Outline each blood parasite and name the species.
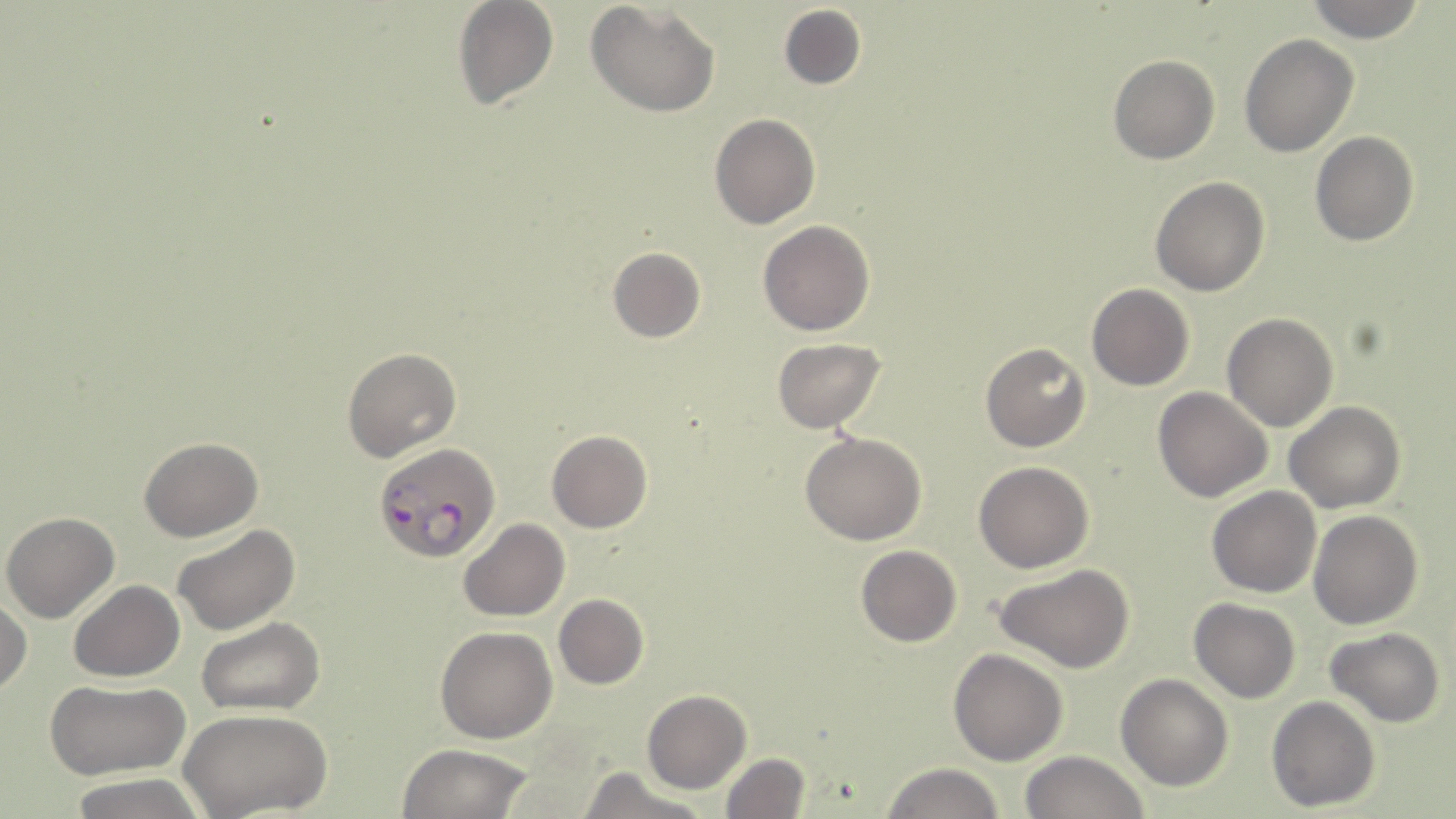
Approximate bounding boxes as [x1, y1, x2, y2] in pixels.
Plasmodium falciparum-infected red blood cells: [371, 442, 501, 562].
No Plasmodium ovale, Plasmodium malariae, Plasmodium vivax, Babesia divergens, or Trypanosoma brucei observed.

Uninfected red blood cell locations: [450, 0, 560, 110], [586, 0, 722, 117], [1307, 0, 1428, 43], [777, 3, 866, 90], [1239, 33, 1358, 157], [1108, 55, 1219, 165], [708, 113, 821, 229], [1310, 132, 1418, 246], [1149, 176, 1271, 297], [757, 220, 875, 336], [609, 247, 707, 343], [1086, 283, 1195, 391], [1223, 312, 1338, 431], [772, 337, 888, 434], [979, 342, 1092, 452], [341, 348, 462, 463], [1152, 386, 1272, 502], [1285, 400, 1404, 513], [547, 430, 652, 532], [800, 430, 927, 546], [140, 436, 264, 541], [973, 461, 1094, 572], [1207, 486, 1322, 598], [1308, 510, 1423, 629], [1, 511, 120, 623], [460, 518, 569, 621], [173, 523, 301, 636], [855, 545, 962, 648], [995, 565, 1134, 673], [69, 580, 184, 682], [553, 594, 650, 690], [0, 595, 30, 699], [1189, 600, 1300, 703], [197, 617, 326, 716], [435, 626, 557, 743], [1324, 628, 1447, 727], [949, 648, 1069, 766], [1116, 673, 1232, 790], [44, 678, 191, 781], [642, 690, 751, 794], [1267, 695, 1380, 811], [180, 708, 332, 817], [395, 742, 536, 819], [1018, 751, 1148, 819], [718, 752, 813, 819], [883, 763, 1005, 819], [575, 767, 709, 819], [68, 775, 205, 819]. Slide-level diagnosis: Plasmodium falciparum. Image is 1456×819 pixels. Thin blood film. One field of a larger specimen. Optical microscopy. 1000x magnification. May-Grünwald-Giemsa-stained preparation.